Classify this cell by malaria status.
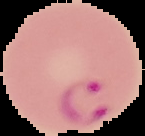

It is parasitized.

{
  "image_type": "segmented cell region on a black background",
  "image_size": "145×136 pixels",
  "preparation": "thin blood smear"
}